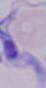

A trypanosome is seen. 1000x magnification. Micrograph.